Describe the morphology of the erythrocytes.
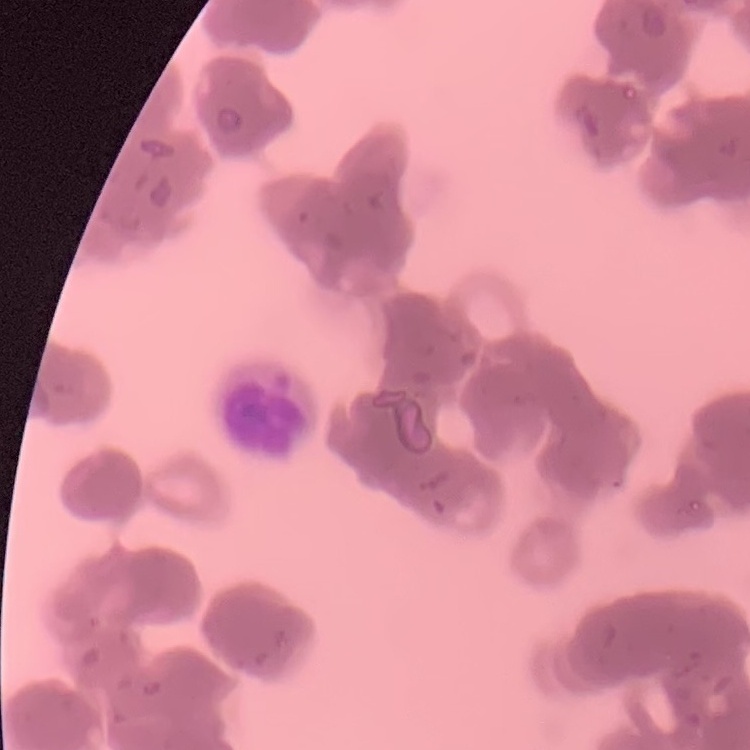
They show rouleaux formation.

image type = one tile cut from a larger photomicrograph
stain = Field's or Giemsa
preparation = thin blood film